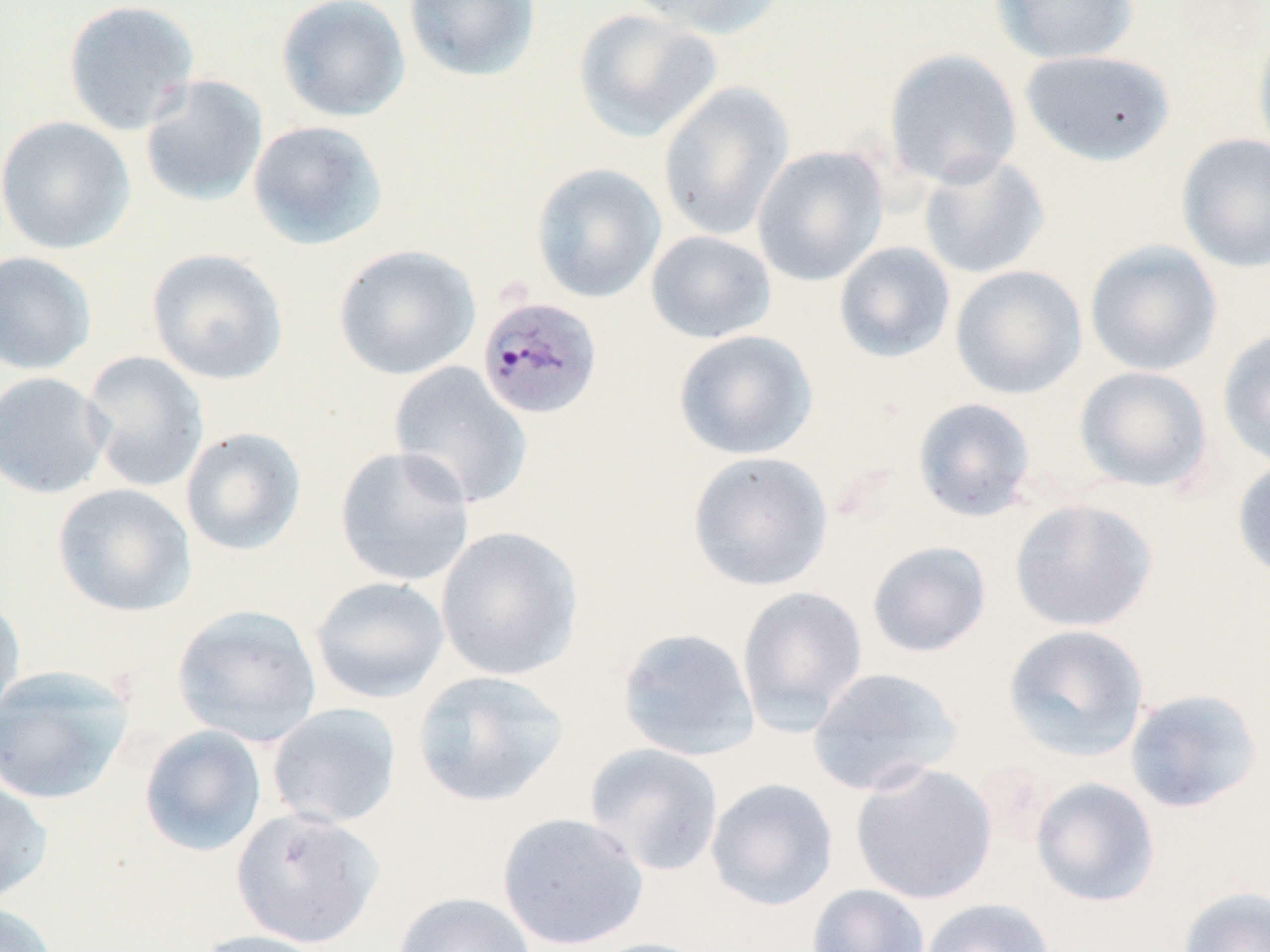
{
  "slide_level_diagnosis": "Plasmodium malariae",
  "stain": "May-Grünwald-Giemsa",
  "plasmodium_malariae_infected_red_blood_cell_locations": "approximate bounding boxes as named x1/y1/x2/y2 corners in pixels: (x1=476, y1=295, x2=604, y2=421)",
  "preparation": "thin blood smear",
  "modality": "light microscopy",
  "image_size": "1270×952 pixels",
  "magnification": "1000x",
  "uninfected_red_blood_cell_locations": "approximate bounding boxes as named x1/y1/x2/y2 corners in pixels: (x1=62, y1=0, x2=200, y2=136), (x1=276, y1=0, x2=411, y2=123), (x1=403, y1=0, x2=541, y2=82), (x1=628, y1=0, x2=788, y2=40), (x1=991, y1=0, x2=1139, y2=65), (x1=572, y1=8, x2=723, y2=142), (x1=1252, y1=19, x2=1270, y2=164), (x1=883, y1=48, x2=1023, y2=189), (x1=1020, y1=49, x2=1175, y2=165), (x1=139, y1=74, x2=269, y2=208), (x1=657, y1=81, x2=795, y2=242), (x1=0, y1=116, x2=135, y2=255), (x1=247, y1=119, x2=390, y2=251), (x1=1176, y1=133, x2=1270, y2=273), (x1=752, y1=145, x2=889, y2=286), (x1=917, y1=152, x2=1050, y2=280), (x1=530, y1=163, x2=667, y2=303), (x1=645, y1=230, x2=776, y2=344), (x1=1084, y1=240, x2=1223, y2=376), (x1=833, y1=242, x2=956, y2=364), (x1=333, y1=244, x2=481, y2=381), (x1=146, y1=248, x2=289, y2=386), (x1=0, y1=251, x2=97, y2=376), (x1=950, y1=265, x2=1087, y2=399), (x1=1217, y1=328, x2=1270, y2=470), (x1=673, y1=329, x2=818, y2=461), (x1=80, y1=350, x2=210, y2=493), (x1=388, y1=361, x2=533, y2=510), (x1=1074, y1=366, x2=1213, y2=493), (x1=0, y1=371, x2=113, y2=500), (x1=912, y1=397, x2=1038, y2=522), (x1=180, y1=426, x2=307, y2=556), (x1=334, y1=446, x2=476, y2=587), (x1=687, y1=451, x2=834, y2=592), (x1=1232, y1=458, x2=1270, y2=582), (x1=51, y1=483, x2=196, y2=617), (x1=1009, y1=498, x2=1158, y2=633), (x1=435, y1=525, x2=583, y2=681), (x1=867, y1=540, x2=992, y2=657), (x1=309, y1=576, x2=450, y2=703), (x1=736, y1=585, x2=868, y2=734), (x1=0, y1=593, x2=25, y2=726), (x1=172, y1=604, x2=323, y2=747), (x1=1002, y1=623, x2=1150, y2=762), (x1=617, y1=626, x2=760, y2=761), (x1=0, y1=665, x2=135, y2=805), (x1=807, y1=666, x2=963, y2=796), (x1=411, y1=669, x2=570, y2=808), (x1=1124, y1=687, x2=1264, y2=814), (x1=266, y1=703, x2=402, y2=829), (x1=138, y1=724, x2=268, y2=857), (x1=584, y1=743, x2=724, y2=877), (x1=850, y1=762, x2=998, y2=905), (x1=0, y1=776, x2=52, y2=906), (x1=705, y1=777, x2=838, y2=911), (x1=1030, y1=777, x2=1160, y2=907), (x1=231, y1=808, x2=384, y2=949), (x1=497, y1=811, x2=649, y2=951), (x1=806, y1=884, x2=930, y2=952), (x1=1178, y1=885, x2=1270, y2=952), (x1=392, y1=892, x2=536, y2=952), (x1=919, y1=897, x2=1056, y2=952), (x1=0, y1=901, x2=62, y2=952), (x1=192, y1=929, x2=335, y2=952), (x1=583, y1=937, x2=719, y2=952)",
  "field_of_view": "one of a larger specimen"
}